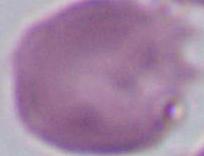
identification: erythrocyte
magnification: 1000x
modality: micrograph